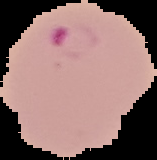 Malaria status: parasitized. From a thin blood smear. Image is 157×160 pixels. The area outside the segmented cell region is set to black.